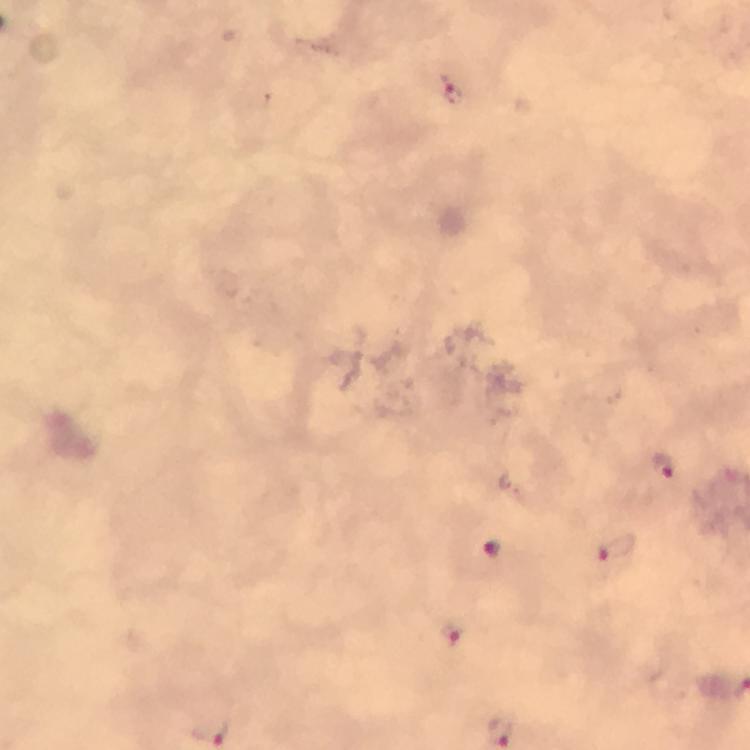
Approximate centers as {x, y} in pixels.
Summary:
  - Malaria parasite locations: {449, 88}, {665, 468}, {617, 548}, {494, 549}, {453, 635}
  - Image size: 750×750 pixels
  - Context: from a diagnostic examination for malaria
  - Stain: Giemsa
  - Magnification: 100x
  - Cropped from: one field of view
  - Immersion oil: used
  - Capture: smartphone mounted on the microscope
  - Preparation: thick blood smear